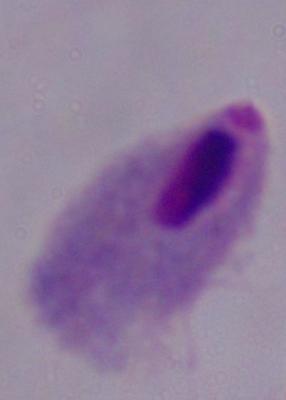

Summary:
  - Identification: trichomonad
  - Magnification: 1000x
  - Modality: photomicrograph